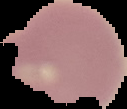
{
  "malaria_status": "uninfected",
  "preparation": "thin blood smear",
  "image_type": "cell region segmented out of the field of view; surrounding area masked to black",
  "image_size": "127×109 pixels"
}